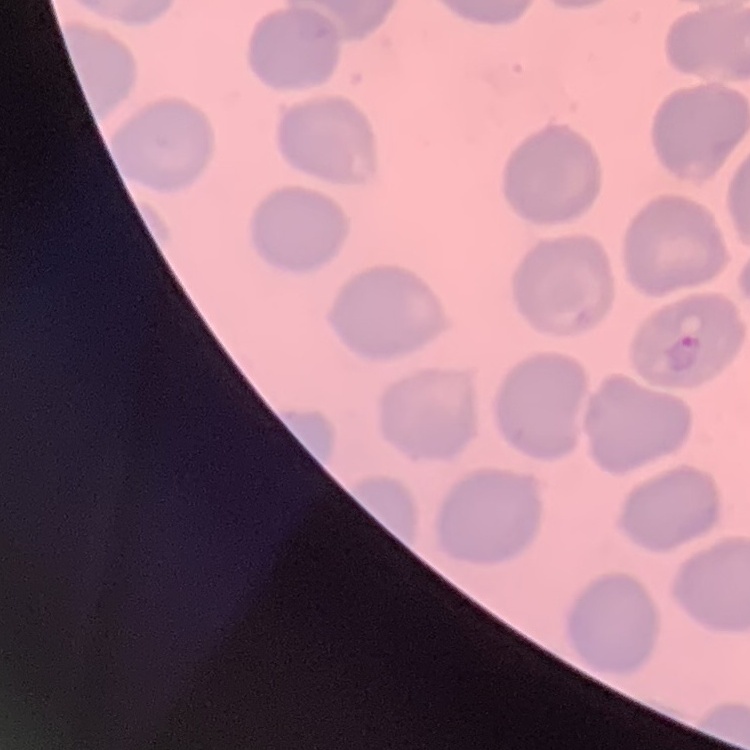

Summary:
  - Red blood cell morphology: no rouleaux formation
  - Image type: square crop of a larger photomicrograph
  - Preparation: thin peripheral smear
  - Stain: Field's or Giemsa